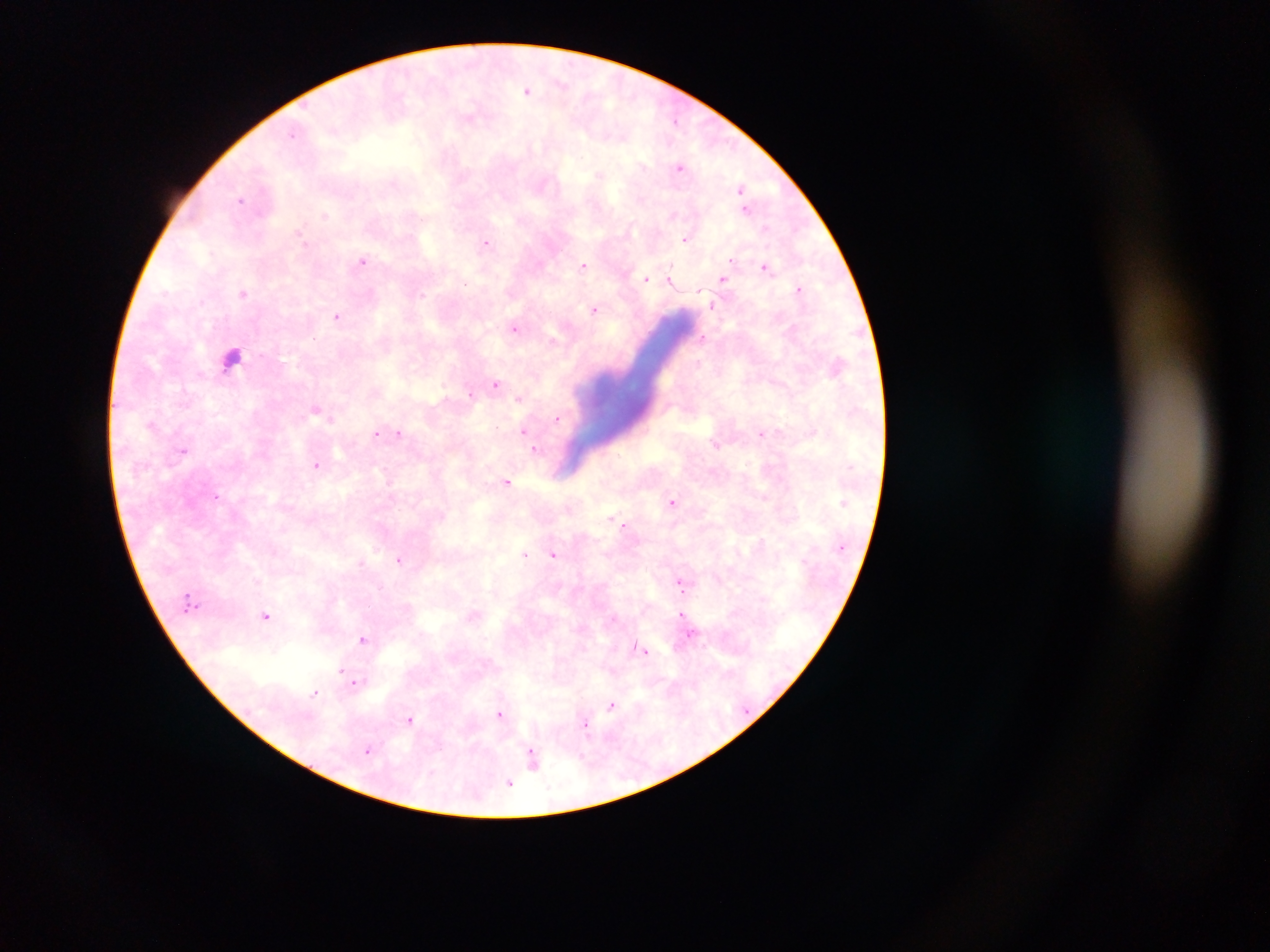 Approximate centers as [x, y] in pixels. Plasmodium parasite locations: [527, 90], [294, 132], [680, 166], [599, 174], [741, 189], [240, 199], [747, 209], [326, 215], [686, 238], [486, 242], [361, 260], [584, 264], [767, 266], [645, 279], [724, 280], [673, 282], [465, 284], [798, 288], [243, 293], [594, 310], [338, 316], [516, 328], [552, 339], [496, 384], [472, 394], [519, 397], [316, 411], [557, 418], [523, 430], [399, 432], [762, 433], [376, 434], [535, 449], [183, 450], [317, 465], [508, 481], [218, 494], [673, 501], [624, 525], [525, 554], [553, 554], [400, 560], [362, 562], [680, 582], [683, 613], [471, 614], [266, 615], [363, 638], [642, 649], [340, 670], [356, 683], [314, 692], [611, 707], [500, 716], [409, 719], [585, 726], [369, 750], [529, 751], [510, 783]. Leukocyte locations: [229, 356]. Image is 1270×952 pixels. Thick blood smear. Sample from Ghana. One field of view. Photographed through a microscope with a mobile-phone camera.